Identify the blood parasite species.
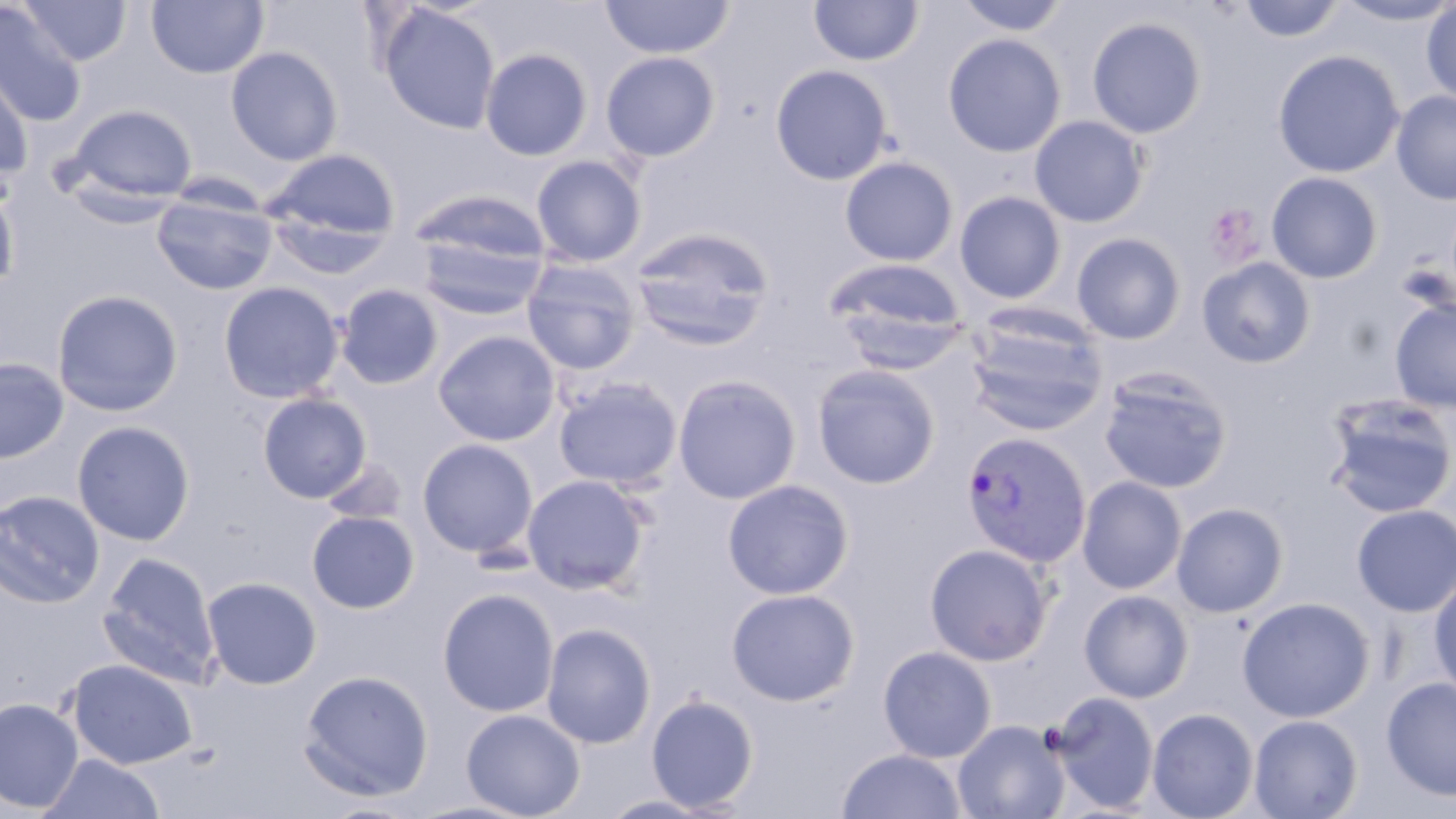

Plasmodium vivax.

modality = light microscopy
platelet locations = approximate bounding boxes as named x1/y1/x2/y2 corners in pixels: (x1=1205, y1=203, x2=1263, y2=265)
stain = May-Grünwald-Giemsa
magnification = 1000x
image size = 1456×819 pixels
field of view = single
Plasmodium vivax-infected red blood cell locations = approximate bounding boxes as named x1/y1/x2/y2 corners in pixels: (x1=960, y1=430, x2=1092, y2=568)
preparation = thin blood smear
uninfected red blood cell locations = approximate bounding boxes as named x1/y1/x2/y2 corners in pixels: (x1=18, y1=0, x2=132, y2=66), (x1=146, y1=0, x2=269, y2=79), (x1=600, y1=0, x2=735, y2=60), (x1=809, y1=0, x2=923, y2=66), (x1=953, y1=0, x2=1072, y2=37), (x1=1237, y1=0, x2=1346, y2=43), (x1=1335, y1=0, x2=1456, y2=26), (x1=1420, y1=2, x2=1456, y2=106), (x1=0, y1=3, x2=88, y2=127), (x1=380, y1=4, x2=501, y2=135), (x1=1086, y1=16, x2=1207, y2=139), (x1=942, y1=32, x2=1066, y2=158), (x1=226, y1=45, x2=343, y2=166), (x1=480, y1=48, x2=593, y2=161), (x1=1272, y1=49, x2=1405, y2=178), (x1=600, y1=51, x2=721, y2=162), (x1=0, y1=53, x2=35, y2=177), (x1=770, y1=63, x2=894, y2=185), (x1=1391, y1=90, x2=1456, y2=205), (x1=63, y1=103, x2=197, y2=208), (x1=1029, y1=115, x2=1149, y2=227), (x1=262, y1=147, x2=401, y2=251), (x1=531, y1=155, x2=647, y2=268), (x1=840, y1=156, x2=959, y2=267), (x1=1266, y1=171, x2=1383, y2=283), (x1=0, y1=180, x2=20, y2=298), (x1=408, y1=190, x2=551, y2=275), (x1=954, y1=190, x2=1067, y2=304), (x1=151, y1=192, x2=278, y2=296), (x1=412, y1=221, x2=550, y2=320), (x1=629, y1=226, x2=776, y2=351), (x1=1072, y1=232, x2=1186, y2=344), (x1=1196, y1=256, x2=1316, y2=368), (x1=824, y1=258, x2=967, y2=358), (x1=521, y1=259, x2=643, y2=375), (x1=1395, y1=260, x2=1455, y2=321), (x1=218, y1=281, x2=344, y2=404), (x1=335, y1=284, x2=444, y2=390), (x1=51, y1=289, x2=184, y2=417), (x1=1389, y1=298, x2=1456, y2=414), (x1=965, y1=311, x2=1108, y2=436), (x1=432, y1=330, x2=560, y2=446), (x1=0, y1=356, x2=69, y2=463), (x1=812, y1=364, x2=940, y2=489), (x1=1098, y1=369, x2=1233, y2=494), (x1=672, y1=374, x2=802, y2=504), (x1=554, y1=377, x2=682, y2=490), (x1=257, y1=392, x2=371, y2=503), (x1=1323, y1=394, x2=1456, y2=518), (x1=71, y1=420, x2=195, y2=546), (x1=417, y1=438, x2=539, y2=558), (x1=321, y1=455, x2=409, y2=526), (x1=521, y1=474, x2=651, y2=594), (x1=1076, y1=476, x2=1188, y2=594), (x1=722, y1=479, x2=854, y2=598), (x1=0, y1=490, x2=105, y2=608), (x1=1171, y1=502, x2=1289, y2=617), (x1=1351, y1=504, x2=1456, y2=617), (x1=306, y1=510, x2=419, y2=613), (x1=924, y1=543, x2=1053, y2=665), (x1=98, y1=552, x2=222, y2=688), (x1=1428, y1=574, x2=1456, y2=699), (x1=201, y1=575, x2=322, y2=689), (x1=726, y1=587, x2=860, y2=706), (x1=437, y1=588, x2=559, y2=717), (x1=1079, y1=589, x2=1194, y2=703), (x1=1237, y1=596, x2=1376, y2=722), (x1=540, y1=622, x2=657, y2=749), (x1=878, y1=645, x2=997, y2=762), (x1=67, y1=658, x2=198, y2=769), (x1=299, y1=669, x2=434, y2=801), (x1=1381, y1=676, x2=1456, y2=801), (x1=1050, y1=691, x2=1159, y2=813), (x1=645, y1=693, x2=759, y2=813), (x1=0, y1=697, x2=83, y2=813), (x1=1147, y1=707, x2=1259, y2=819), (x1=461, y1=709, x2=585, y2=818), (x1=1248, y1=714, x2=1362, y2=819), (x1=953, y1=719, x2=1069, y2=819), (x1=836, y1=748, x2=967, y2=819), (x1=40, y1=755, x2=164, y2=818), (x1=598, y1=793, x2=721, y2=818)